Identify the parasite.
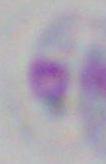

Toxoplasma gondii.

{
  "magnification": "1000x",
  "modality": "micrograph"
}